Assess this cell for malaria.
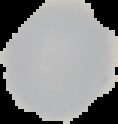
Uninfected.

Summary:
  - Image type: cell region segmented out of the field of view; surrounding area masked to black
  - Image size: 118×124 pixels
  - Preparation: thin blood film